State the blood parasite species.
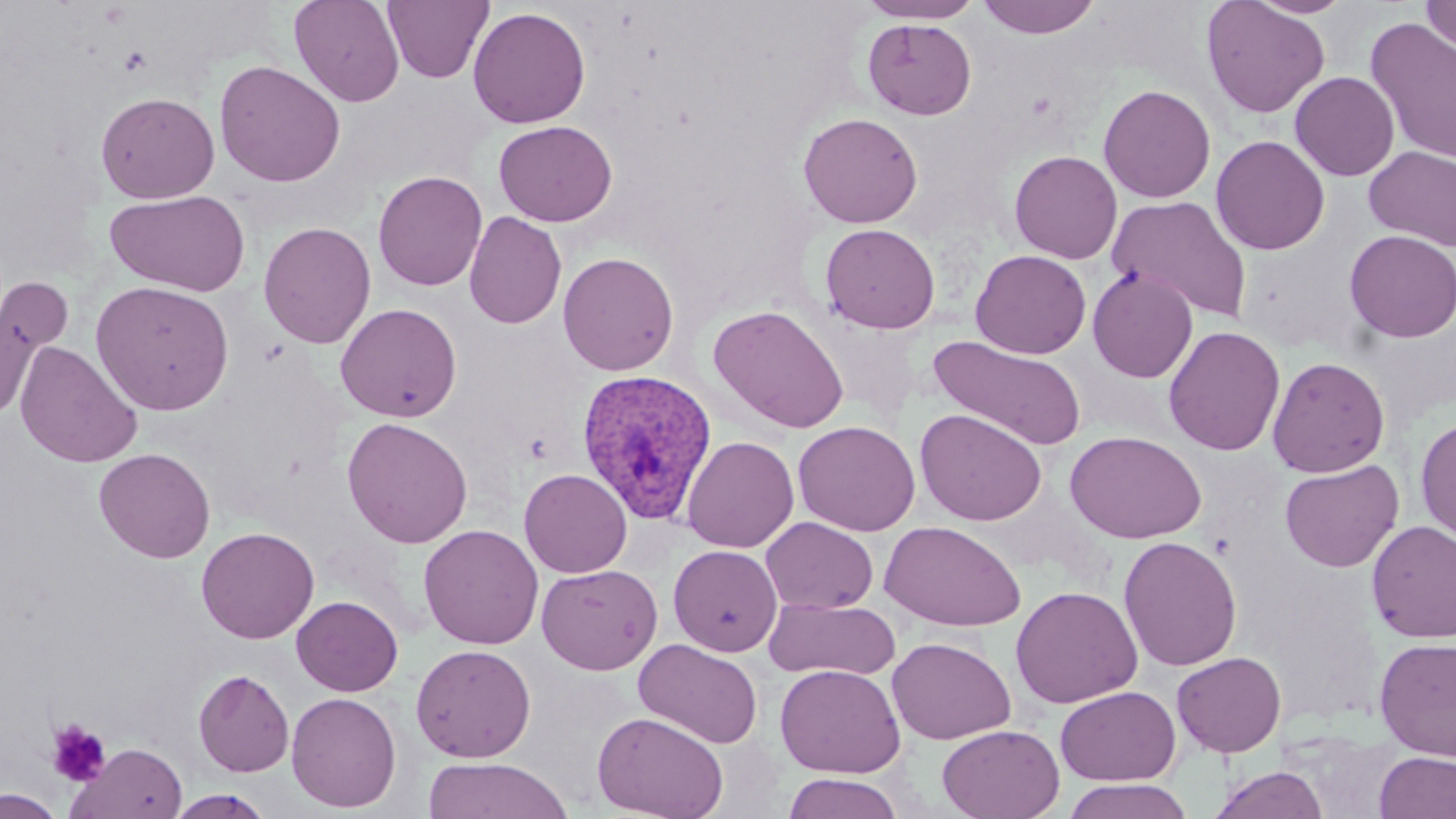
Plasmodium vivax.

Approximate bounding boxes as (x1, y1, x2, y2) in pixels. Uninfected red blood cell locations: (289, 0, 405, 107), (382, 0, 494, 84), (859, 0, 981, 23), (977, 0, 1101, 38), (1200, 0, 1330, 119), (1248, 0, 1355, 18), (1421, 0, 1455, 56), (467, 6, 591, 129), (1364, 17, 1456, 165), (862, 18, 977, 120), (213, 59, 346, 187), (1290, 71, 1400, 181), (1098, 84, 1216, 203), (96, 92, 220, 203), (798, 112, 923, 228), (493, 120, 617, 226), (1210, 134, 1330, 255), (1363, 145, 1456, 252), (1009, 150, 1123, 263), (372, 170, 487, 291), (105, 190, 251, 296), (1107, 195, 1253, 323), (464, 210, 566, 329), (258, 221, 376, 348), (820, 222, 940, 333), (1343, 230, 1456, 342), (970, 249, 1091, 359), (557, 251, 679, 376), (1087, 267, 1198, 382), (0, 277, 66, 420), (90, 280, 235, 416), (335, 302, 462, 422), (708, 304, 849, 434), (1163, 325, 1285, 456), (929, 335, 1087, 450), (15, 341, 143, 467), (1267, 356, 1390, 477), (915, 408, 1047, 526), (1415, 414, 1456, 546), (341, 416, 473, 548), (792, 420, 920, 536), (1064, 430, 1207, 543), (681, 435, 799, 552), (94, 447, 215, 563), (1279, 459, 1404, 572), (519, 468, 632, 577), (761, 516, 878, 613), (1366, 520, 1456, 643), (879, 521, 1026, 632), (419, 524, 543, 649), (196, 526, 319, 643), (1118, 535, 1242, 672), (668, 544, 782, 656), (536, 564, 663, 674), (1010, 585, 1142, 709), (291, 595, 403, 696), (764, 596, 901, 681), (886, 636, 1016, 744), (1374, 637, 1456, 760), (633, 638, 763, 748), (411, 643, 537, 762), (1172, 652, 1287, 757), (775, 664, 906, 778), (193, 669, 294, 776), (1055, 686, 1181, 785), (286, 691, 402, 812), (591, 710, 729, 819), (937, 724, 1065, 819), (68, 742, 188, 819), (1374, 751, 1456, 818), (421, 756, 574, 819), (1207, 765, 1330, 819), (781, 773, 904, 818), (1060, 778, 1197, 819), (1, 789, 65, 818), (166, 790, 275, 818). Platelet locations: (119, 45, 152, 75), (47, 720, 111, 787). Plasmodium vivax-infected red blood cell locations: (575, 368, 718, 525). Single field of view. May-Grünwald-Giemsa-stained preparation. Thin blood smear. 1000x magnification. Image is 1456×819 pixels. Light microscopy.